Describe the morphology of the red blood cells.
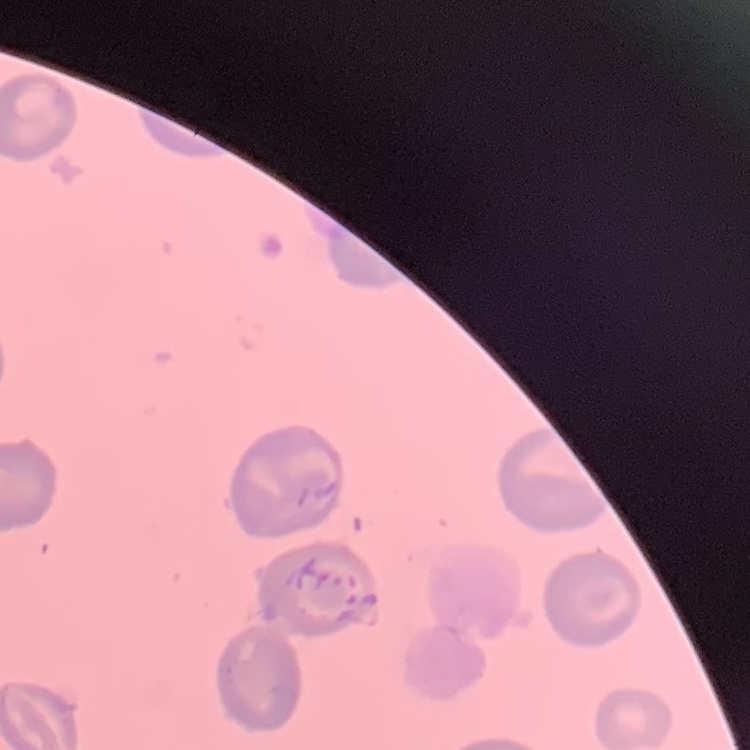
They show no rouleaux formation.

Summary:
  - Image type: one tile cut from a larger photomicrograph
  - Stain: Field's or Giemsa
  - Preparation: thin blood film